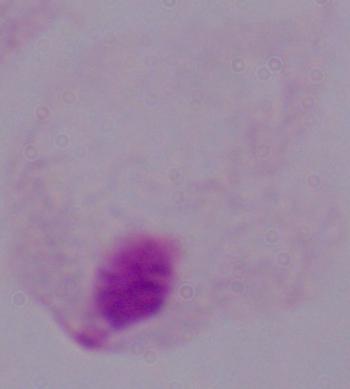
Summary:
  - Modality: micrograph
  - Identification: trichomonad
  - Magnification: 1000x